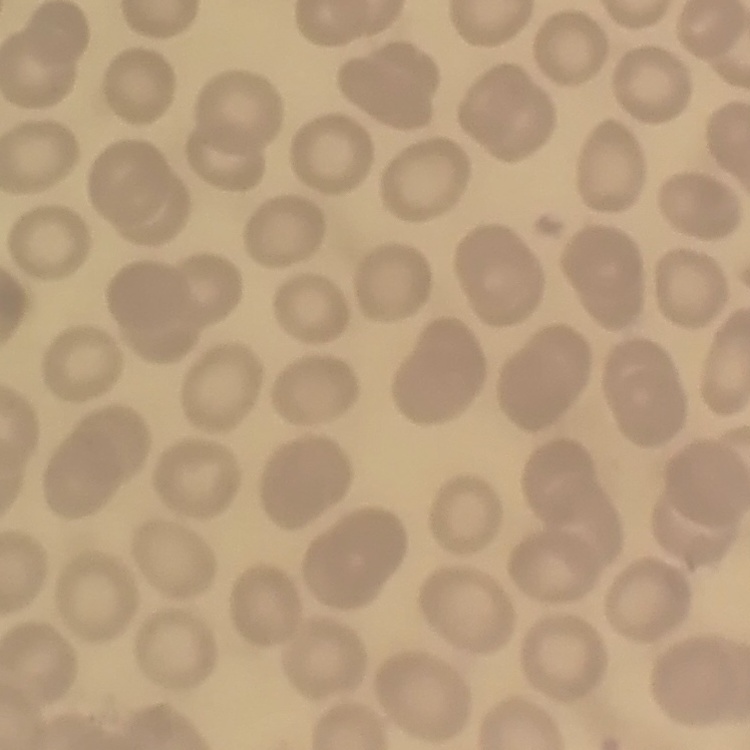 The erythrocytes exhibit no rouleaux formation. Square crop of a larger photomicrograph. Thin peripheral smear. Field's or Giemsa stain.